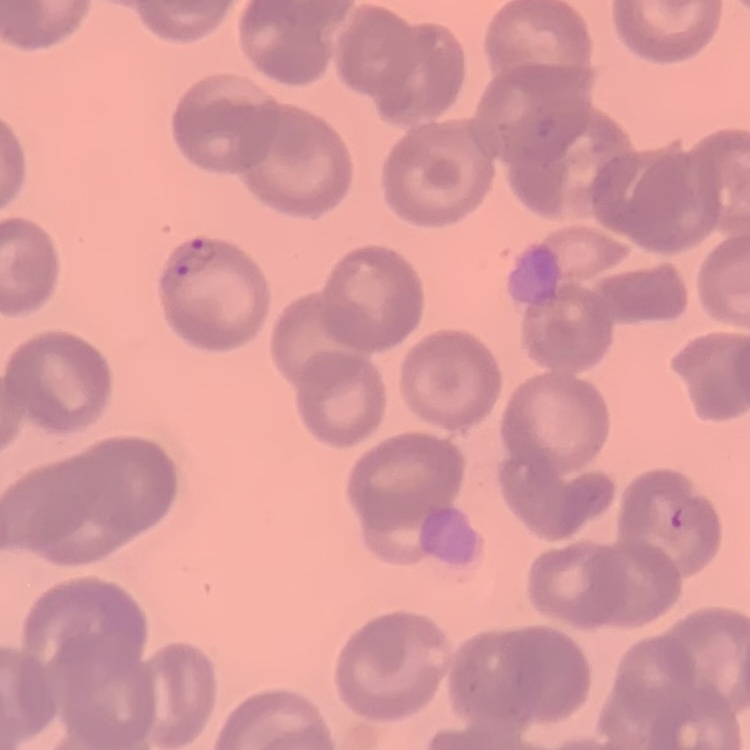

{
  "erythrocyte_morphology": "no rouleaux formation",
  "stain": "Field's or Giemsa",
  "preparation": "thin peripheral smear",
  "image_type": "one tile cut from a larger photomicrograph"
}